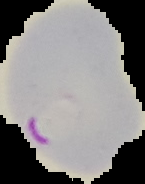
Summary:
  - Result: Plasmodium parasites identified
  - Preparation: thin blood film
  - Image size: 145×184 pixels
  - Image type: cell region segmented out of the field of view; surrounding area masked to black